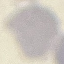

Summary:
  - Malaria status: uninfected
  - Stain: Giemsa
  - Image type: automatically extracted cell patch, resized to 64 × 64 pixels
  - Preparation: thin smear
  - Capture: smartphone camera at the microscope eyepiece